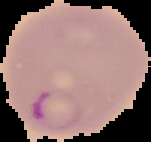

Image is 151×142 pixels. Result: Plasmodium parasites identified. From a thin blood film. Cell region segmented out of the field of view; the surrounding area is masked to black.